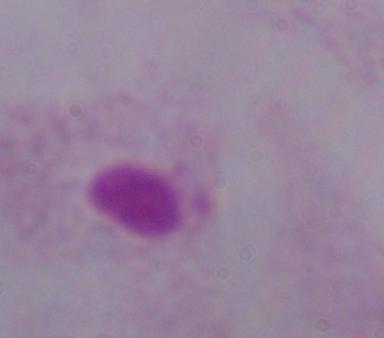
modality = micrograph
identification = trichomonad
magnification = 1000x